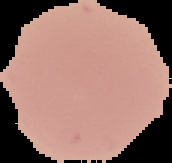

Summary:
  - Result: negative for malaria parasites
  - Image type: segmented cell region with the area outside set to black
  - Preparation: thin blood film
  - Image size: 172×163 pixels